State the blood parasite species.
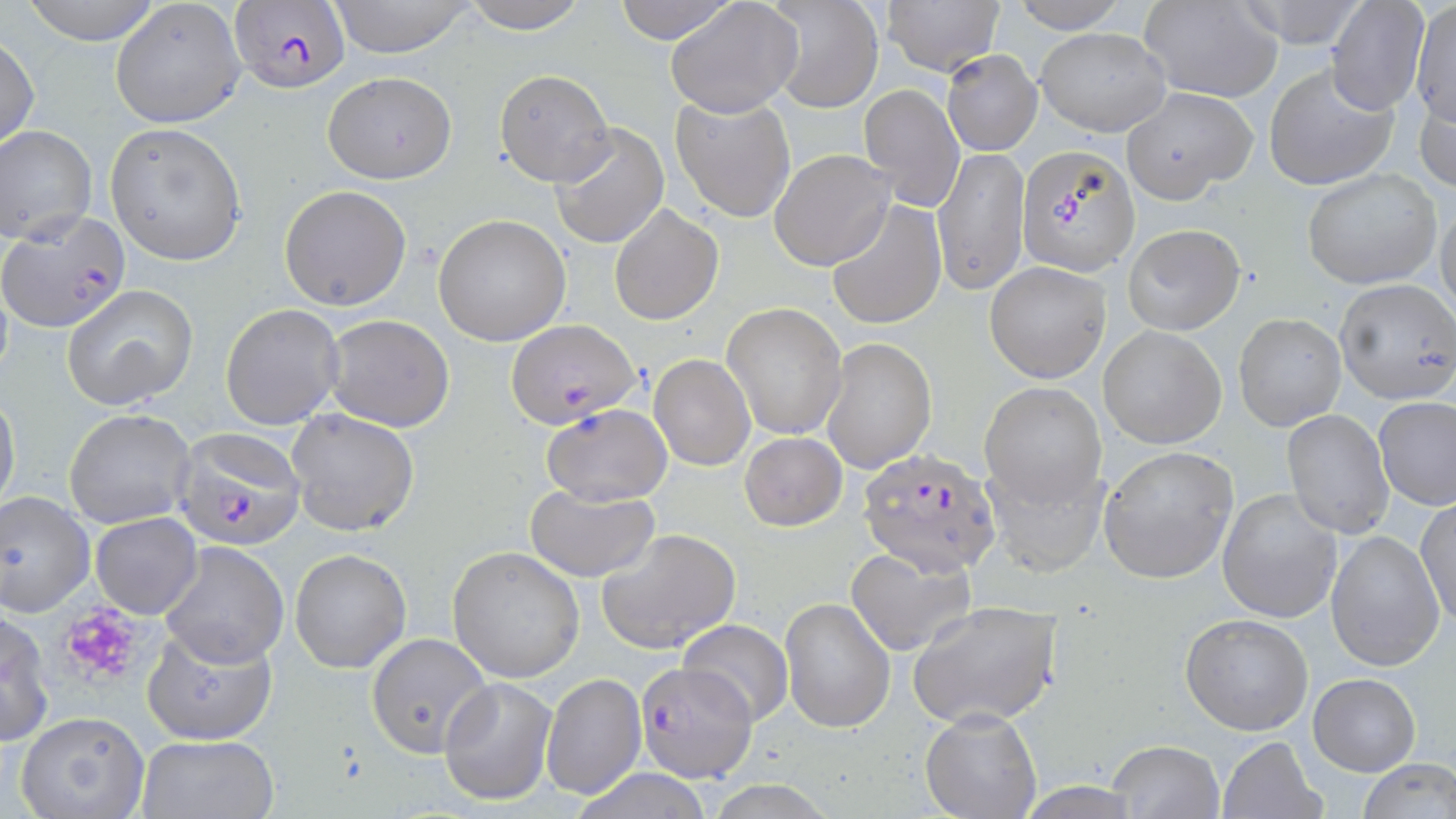
Plasmodium falciparum.

Summary:
  - Coordinate format: approximate bounding boxes as [x1, y1, x2, y2] in pixels
  - Uninfected red blood cell locations: [19, 0, 166, 45], [457, 0, 590, 34], [610, 0, 740, 45], [666, 0, 802, 118], [880, 0, 1005, 75], [1005, 0, 1132, 33], [1141, 0, 1284, 102], [1227, 0, 1368, 48], [1324, 0, 1432, 115], [1411, 0, 1456, 130], [110, 1, 246, 130], [327, 1, 479, 58], [765, 3, 883, 112], [1034, 28, 1172, 135], [0, 34, 39, 154], [941, 50, 1041, 156], [1264, 62, 1399, 192], [492, 69, 615, 186], [322, 72, 457, 185], [1417, 81, 1456, 200], [861, 83, 965, 210], [1121, 86, 1256, 202], [669, 93, 797, 224], [103, 123, 248, 265], [550, 123, 670, 248], [1, 126, 97, 247], [933, 146, 1029, 295], [769, 148, 894, 271], [1302, 168, 1440, 289], [279, 185, 412, 311], [1435, 197, 1455, 324], [826, 200, 946, 331], [608, 202, 723, 326], [432, 213, 571, 345], [1122, 223, 1245, 335], [984, 262, 1112, 384], [1335, 278, 1456, 406], [62, 285, 197, 410], [722, 302, 848, 441], [221, 303, 346, 431], [1233, 313, 1346, 430], [323, 315, 455, 431], [1098, 325, 1226, 449], [821, 337, 936, 474], [648, 354, 756, 473], [981, 383, 1106, 508], [0, 389, 21, 517], [1374, 397, 1456, 509], [540, 403, 672, 505], [64, 408, 195, 529], [286, 409, 419, 536], [1281, 409, 1394, 538], [738, 432, 848, 531], [1099, 444, 1239, 584], [983, 455, 1108, 577], [525, 483, 659, 580], [0, 489, 95, 620], [1218, 489, 1344, 623], [1415, 497, 1455, 628], [90, 513, 201, 620], [597, 528, 741, 655], [1326, 528, 1445, 671], [159, 540, 289, 667], [846, 544, 978, 658], [289, 548, 412, 674], [447, 548, 586, 683], [780, 596, 894, 733], [908, 600, 1064, 728], [1, 607, 55, 747], [1180, 613, 1313, 736], [677, 618, 796, 727], [141, 625, 279, 746], [366, 633, 490, 757], [540, 672, 646, 800], [1308, 673, 1421, 775], [439, 676, 558, 806], [919, 707, 1043, 818], [13, 709, 151, 819], [133, 734, 278, 818], [1217, 736, 1325, 819], [1105, 739, 1226, 818], [1354, 759, 1455, 818]
  - Platelet locations: [55, 604, 151, 690]
  - Plasmodium falciparum-infected red blood cell locations: [230, 0, 352, 90], [1017, 144, 1137, 278], [1, 211, 132, 334], [507, 318, 641, 427], [173, 428, 305, 550], [859, 449, 1005, 575], [633, 662, 755, 783]
  - Preparation: thin blood film
  - Field of view: one of a larger specimen
  - Magnification: 1000x
  - Stain: May-Grünwald-Giemsa
  - Image size: 1456×819 pixels
  - Modality: light microscopy